Assess this cell for malaria.
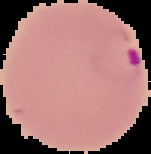

Parasitized.

From a thin blood smear. Image is 151×154 pixels. The area outside the segmented cell region is set to black.